Describe the morphology of the erythrocytes.
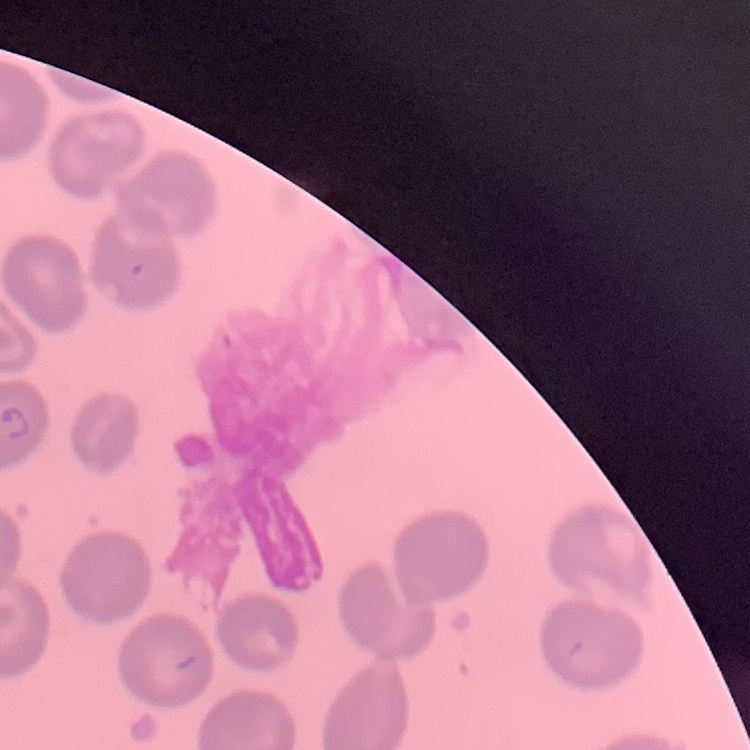
No rouleaux formation.

Field's or Giemsa stain. Thin blood smear. One tile cut from a larger photomicrograph.